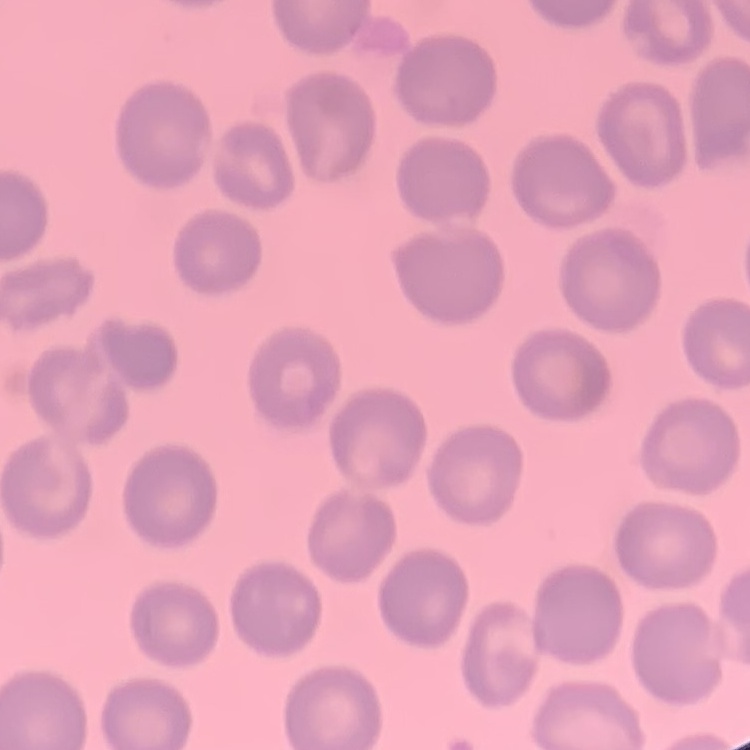 The red blood cells show no rouleaux formation. Thin blood film. One tile cut from a larger photomicrograph. Stained with either Field's or Giemsa.